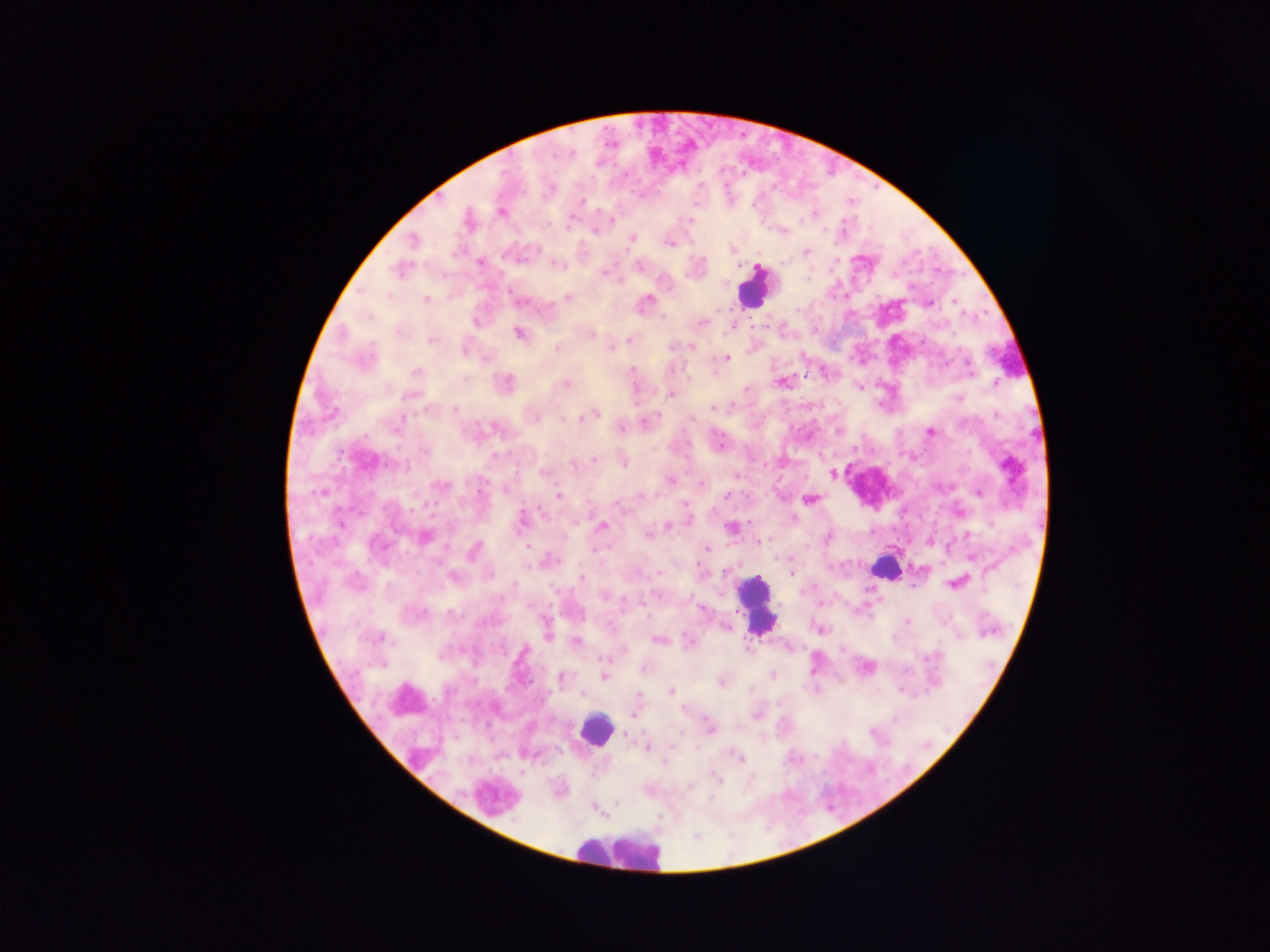
leukocyte locations = approximate centers as {x, y} in pixels: {754, 287}, {884, 567}, {756, 604}, {596, 729}, {618, 851}
image size = 1270×952 pixels
field of view = single
Plasmodium parasite locations = approximate centers as {x, y} in pixels: {501, 211}, {610, 219}, {467, 220}, {689, 220}, {571, 221}, {596, 230}, {781, 231}, {631, 239}, {413, 241}, {671, 243}, {731, 250}, {806, 251}, {480, 263}, {557, 264}, {638, 265}, {604, 273}, {567, 298}, {426, 299}, {646, 301}, {518, 302}, {928, 303}, {702, 322}, {732, 326}, {518, 333}, {589, 333}, {432, 339}, {631, 339}, {691, 346}, {610, 347}, {557, 348}, {464, 350}, {725, 358}, {486, 359}, {632, 371}, {782, 381}, {505, 384}, {567, 384}, {994, 384}, {671, 394}, {959, 397}, {713, 407}, {592, 413}, {535, 415}, {996, 415}, {646, 422}, {621, 429}, {837, 430}, {931, 432}, {819, 456}, {594, 458}, {622, 461}, {575, 463}, {542, 472}, {832, 473}, {670, 480}, {702, 484}, {439, 486}, {505, 489}, {979, 492}, {725, 495}, {559, 496}, {809, 499}, {685, 504}, {956, 512}, {522, 521}, {601, 526}, {667, 526}, {731, 527}, {648, 534}, {423, 536}, {757, 542}, {930, 542}, {705, 549}, {473, 550}, {971, 556}, {547, 561}, {923, 568}, {790, 573}, {452, 577}, {582, 578}, {957, 582}, {912, 585}, {701, 609}, {907, 621}, {819, 629}, {548, 633}, {378, 637}, {658, 639}, {576, 640}, {689, 642}, {788, 646}, {866, 667}, {644, 668}, {773, 675}, {604, 676}, {560, 678}, {721, 682}, {670, 691}, {584, 694}, {634, 714}, {757, 714}, {709, 728}, {625, 733}, {646, 747}, {737, 757}, {665, 763}, {716, 779}, {594, 808}
preparation = thick blood smear
capture = mobile-phone photograph through a microscope
country = Ghana